Outline each uninfected red blood cell.
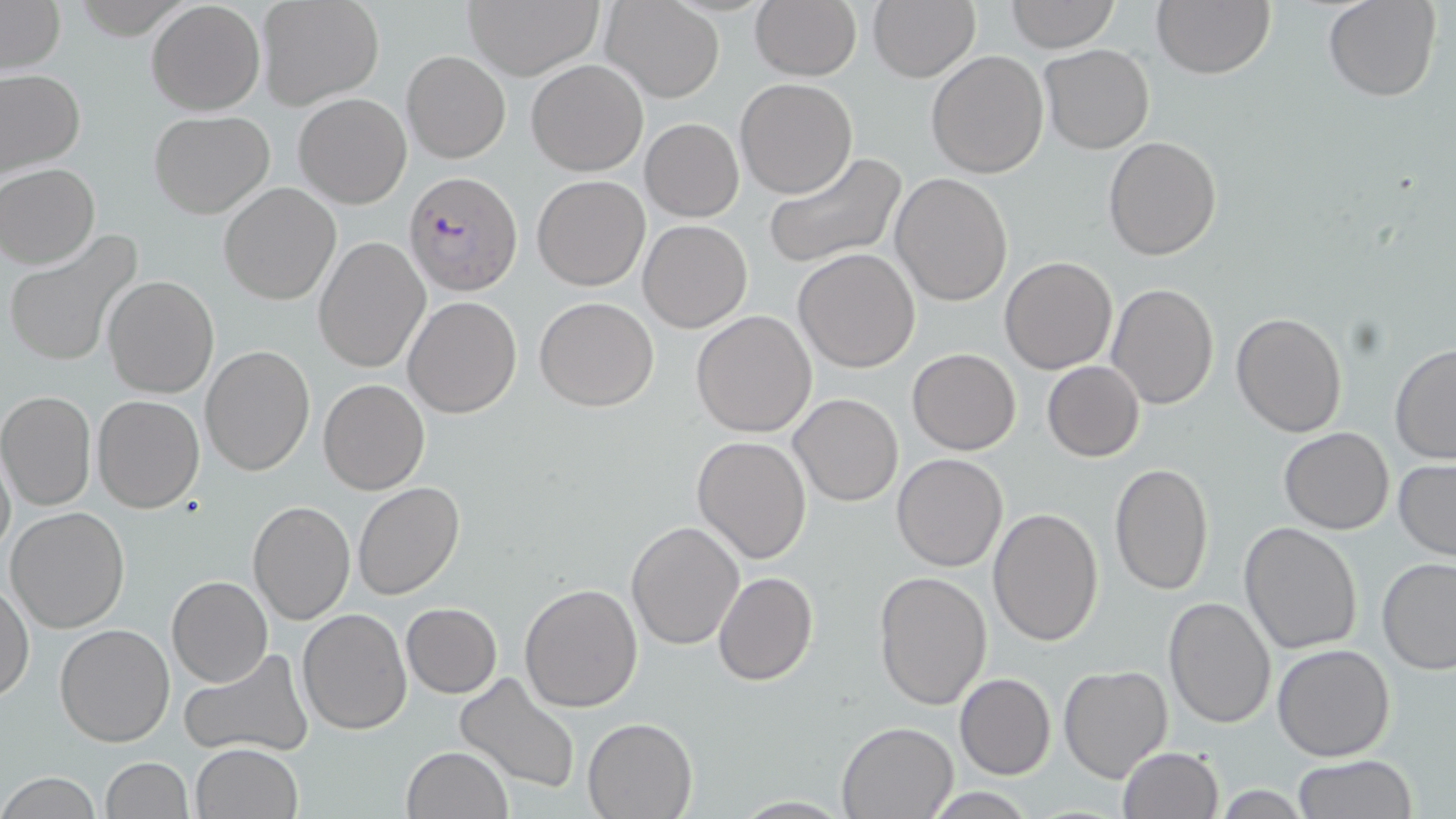
Approximate bounding boxes as [x1, y1, x2, y2] in pixels.
Uninfected red blood cells: [258, 0, 385, 110], [602, 0, 724, 102], [749, 0, 862, 81], [1006, 0, 1118, 52], [1151, 0, 1275, 80], [1323, 0, 1440, 102], [0, 1, 65, 74], [464, 1, 602, 79], [147, 2, 264, 115], [868, 2, 980, 82], [1039, 44, 1155, 155], [402, 49, 510, 163], [926, 49, 1049, 178], [526, 59, 648, 175], [0, 68, 85, 179], [734, 78, 858, 199], [293, 93, 412, 208], [148, 110, 275, 218], [641, 118, 743, 221], [1103, 136, 1221, 259], [764, 152, 905, 269], [2, 163, 100, 268], [890, 173, 1013, 306], [532, 175, 649, 292], [219, 183, 341, 304], [639, 220, 752, 333], [4, 234, 141, 367], [313, 237, 429, 373], [794, 248, 922, 372], [1000, 256, 1117, 374], [102, 275, 218, 397], [1107, 282, 1219, 410], [404, 296, 523, 419], [534, 297, 659, 411], [690, 310, 818, 438], [1231, 312, 1347, 437], [199, 345, 315, 476], [1389, 345, 1456, 465], [907, 348, 1021, 455], [1042, 361, 1144, 462], [319, 378, 429, 494], [0, 391, 97, 511], [92, 393, 204, 513], [789, 393, 904, 508], [1279, 427, 1394, 534], [692, 436, 813, 564], [0, 438, 14, 565], [892, 453, 1008, 572], [1394, 460, 1456, 561], [1108, 461, 1214, 597], [352, 483, 465, 601], [248, 501, 354, 624], [5, 505, 131, 632], [987, 509, 1105, 647], [626, 520, 745, 651], [1240, 521, 1364, 654], [1375, 557, 1456, 673], [874, 570, 993, 709], [713, 571, 819, 685], [167, 575, 273, 687], [0, 580, 34, 703], [519, 583, 643, 712], [1162, 597, 1276, 729], [401, 603, 502, 698], [297, 608, 411, 734], [55, 624, 174, 746], [1272, 644, 1395, 762], [178, 650, 313, 758], [1059, 665, 1173, 782], [454, 672, 582, 794], [954, 672, 1056, 779], [583, 717, 698, 818], [836, 721, 958, 818], [192, 743, 304, 819], [400, 746, 512, 819], [1117, 746, 1223, 819], [1294, 754, 1419, 818], [100, 757, 192, 818], [0, 773, 103, 817], [922, 788, 1037, 819].

Summary:
  - Plasmodium falciparum-infected red blood cell locations: [404, 172, 520, 296]
  - Slide-level diagnosis: Plasmodium falciparum
  - Magnification: 1000x
  - Field of view: single
  - Image size: 1456×819 pixels
  - Stain: May-Grünwald-Giemsa
  - Modality: light microscopy
  - Preparation: thin blood film